Locate every blood parasite and identify its species.
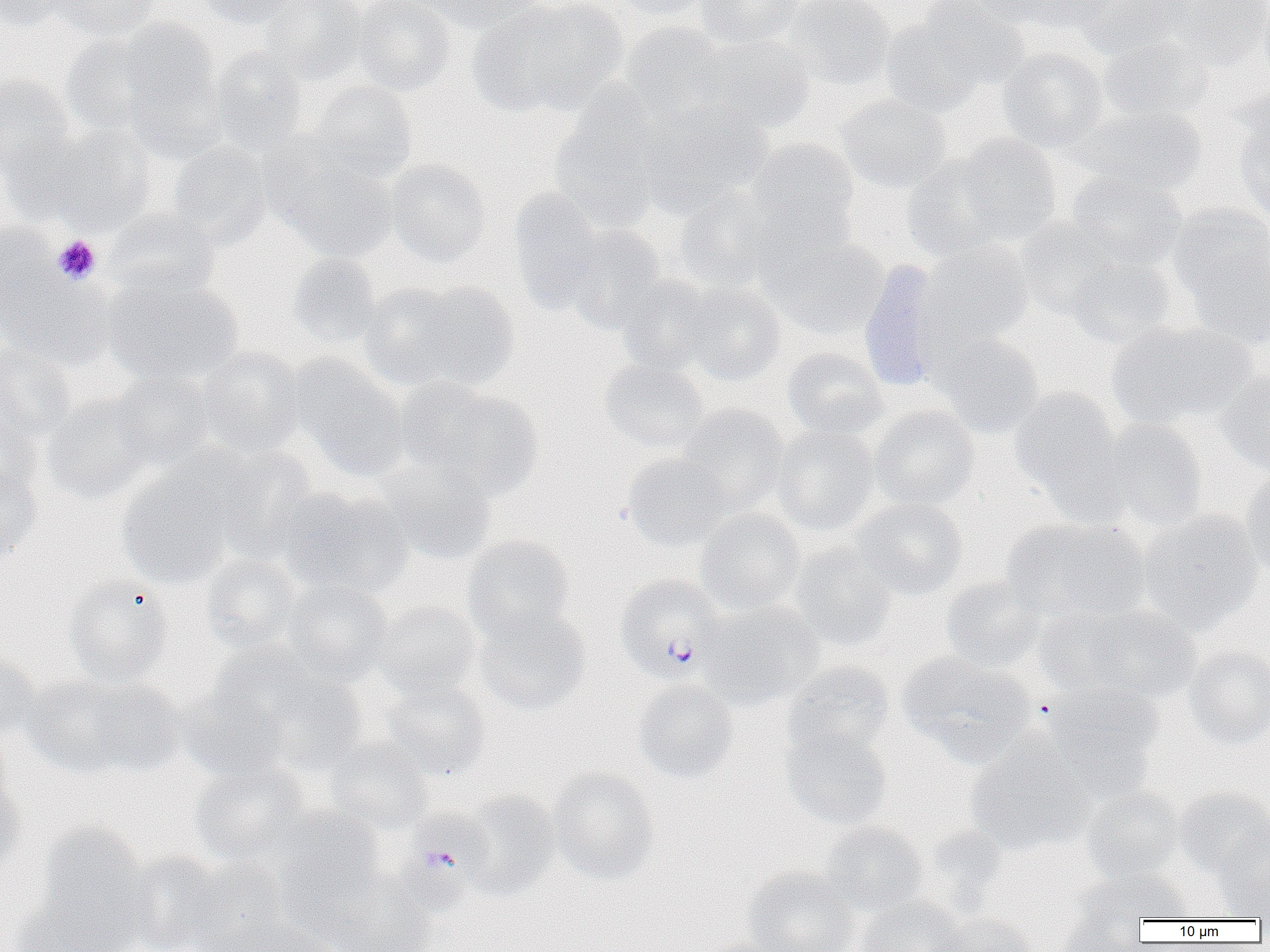

Approximate bounding boxes as (x1, y1, x2, y2) in pixels.
Plasmodium falciparum-infected red blood cells: (615, 575, 725, 682), (385, 812, 491, 918).
No Plasmodium ovale, Plasmodium malariae, Plasmodium vivax, Babesia divergens, or Trypanosoma brucei observed.

Uninfected red blood cell locations: (0, 0, 71, 32), (48, 0, 160, 41), (193, 0, 301, 28), (257, 0, 367, 84), (352, 0, 456, 95), (422, 0, 547, 34), (468, 0, 627, 117), (609, 0, 711, 21), (696, 0, 807, 48), (782, 0, 895, 91), (968, 0, 1075, 28), (997, 0, 1119, 34), (1076, 0, 1193, 59), (1167, 0, 1270, 73), (913, 1, 1030, 92), (881, 16, 987, 119), (115, 19, 222, 131), (620, 21, 732, 123), (60, 32, 165, 135), (696, 34, 816, 135), (1099, 35, 1214, 123), (211, 46, 309, 154), (997, 47, 1109, 152), (0, 73, 75, 176), (306, 80, 418, 184), (549, 92, 666, 233), (835, 94, 951, 193), (638, 100, 774, 216), (1078, 104, 1205, 196), (1235, 111, 1270, 223), (46, 126, 157, 234), (1, 133, 93, 226), (954, 134, 1062, 244), (745, 138, 858, 236), (167, 141, 274, 250), (273, 150, 398, 263), (901, 154, 1014, 262), (385, 159, 491, 267), (1065, 171, 1188, 271), (507, 188, 610, 313), (673, 188, 782, 292), (1167, 205, 1270, 308), (106, 209, 219, 298), (1014, 218, 1122, 320), (0, 221, 59, 324), (560, 225, 667, 333), (768, 236, 888, 340), (919, 241, 1034, 349), (1186, 244, 1270, 350), (287, 253, 382, 348), (1064, 256, 1177, 348), (857, 260, 947, 393), (1, 270, 115, 371), (615, 274, 724, 374), (103, 275, 244, 388), (678, 280, 786, 385), (392, 281, 519, 392), (1106, 321, 1256, 429), (931, 330, 1044, 437), (0, 343, 76, 441), (198, 347, 306, 458), (781, 348, 887, 441), (288, 355, 408, 479), (599, 359, 709, 452), (1216, 367, 1270, 477), (110, 371, 216, 469), (397, 380, 542, 499), (1009, 387, 1123, 500), (44, 393, 157, 505), (676, 404, 790, 517), (868, 405, 979, 512), (0, 415, 44, 508), (1094, 418, 1208, 533), (771, 424, 879, 537), (208, 448, 318, 563), (623, 452, 732, 551), (377, 458, 498, 565), (0, 467, 43, 562), (116, 467, 236, 590), (1240, 471, 1270, 578), (277, 487, 413, 601), (852, 497, 968, 599), (694, 508, 805, 614), (1138, 510, 1264, 634), (1002, 516, 1152, 624), (462, 535, 575, 640), (789, 544, 895, 652), (199, 555, 303, 654), (63, 575, 175, 687), (941, 577, 1045, 672), (281, 580, 395, 685), (373, 600, 482, 702), (699, 601, 824, 709), (1056, 603, 1203, 704), (473, 606, 591, 716), (1185, 646, 1270, 748), (0, 649, 41, 741), (221, 651, 367, 775), (898, 652, 1034, 766), (783, 660, 895, 759), (22, 675, 182, 778), (381, 679, 492, 780), (1044, 679, 1163, 795), (633, 680, 739, 783), (179, 683, 292, 784), (780, 727, 893, 830), (965, 733, 1094, 856), (324, 738, 435, 835), (189, 761, 312, 868), (547, 768, 660, 885), (0, 770, 25, 876), (1080, 786, 1187, 884), (1174, 788, 1270, 879), (457, 790, 560, 900), (267, 804, 385, 911), (820, 821, 928, 915), (35, 823, 149, 942), (1213, 826, 1270, 918), (123, 851, 233, 952), (182, 859, 290, 951), (743, 866, 859, 952), (1076, 868, 1194, 923), (329, 875, 438, 952), (11, 895, 134, 952), (854, 895, 966, 952), (1058, 899, 1148, 952), (933, 912, 1037, 952), (219, 920, 338, 952), (693, 938, 791, 952). Platelet locations: (52, 235, 101, 285). Slide-level diagnosis: Plasmodium falciparum. Thin blood film. Image is 1270×952 pixels. Single field of view. 1000x magnification. Optical microscopy.